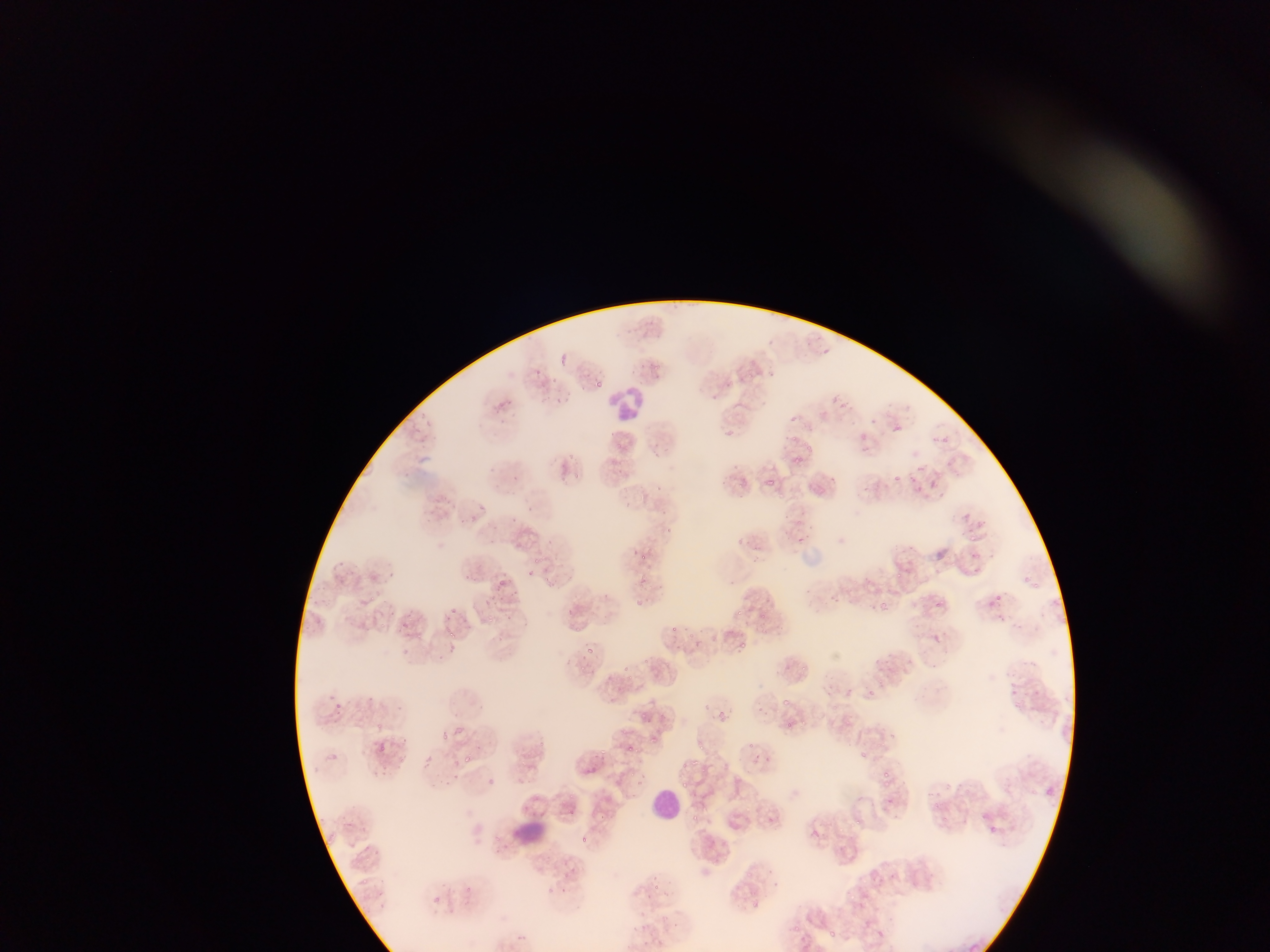

Approximate bounding boxes as [left, top, right, bottom] in pixels.
Summary:
  - Malaria parasite locations: [554, 352, 569, 367], [650, 362, 661, 372], [597, 380, 603, 391], [789, 432, 796, 442], [805, 444, 813, 453], [567, 452, 576, 460], [795, 457, 805, 467], [572, 472, 586, 479], [892, 473, 901, 483], [765, 477, 775, 488], [478, 503, 487, 509], [468, 513, 476, 519], [667, 526, 676, 534], [970, 535, 976, 543], [533, 553, 550, 565], [639, 553, 649, 560], [527, 568, 533, 583], [896, 571, 902, 582], [641, 573, 651, 583], [1022, 573, 1031, 583], [492, 575, 511, 593], [1031, 581, 1042, 590], [994, 593, 1004, 603], [368, 596, 381, 605], [632, 597, 647, 607], [880, 599, 891, 611], [933, 600, 943, 610], [444, 606, 458, 614], [734, 606, 742, 614], [759, 610, 768, 618], [487, 611, 498, 622], [381, 620, 390, 629], [667, 623, 681, 635], [573, 624, 579, 634], [445, 626, 456, 637], [418, 632, 428, 639], [741, 641, 750, 650], [586, 645, 599, 658], [623, 663, 635, 676], [801, 663, 809, 672], [578, 665, 592, 675], [867, 689, 878, 701], [783, 700, 791, 709], [718, 710, 727, 725], [641, 712, 653, 724], [779, 716, 799, 734], [374, 721, 384, 727], [455, 723, 467, 740], [438, 729, 447, 740], [649, 735, 659, 745], [368, 738, 392, 760], [748, 739, 755, 751], [695, 742, 706, 752], [623, 743, 634, 751], [599, 744, 612, 760], [858, 749, 867, 758], [465, 754, 477, 764], [400, 756, 409, 767], [695, 758, 704, 771], [680, 764, 693, 771], [880, 769, 892, 776], [629, 771, 637, 778], [681, 780, 690, 789], [879, 780, 894, 789], [945, 781, 953, 790], [1043, 787, 1054, 799], [932, 800, 943, 810], [565, 807, 578, 821], [980, 813, 999, 836], [692, 814, 701, 824], [851, 816, 863, 827], [578, 834, 593, 846], [360, 876, 372, 886], [466, 884, 476, 895], [652, 884, 662, 894], [751, 902, 761, 908], [793, 923, 803, 934], [828, 928, 836, 938]
  - Leukocyte locations: [609, 384, 646, 426], [639, 778, 680, 832], [516, 814, 553, 852]
  - Field of view: single
  - Image size: 1270×952 pixels
  - Preparation: thin blood film
  - Capture: mobile-phone photograph through a microscope
  - Country: Ghana